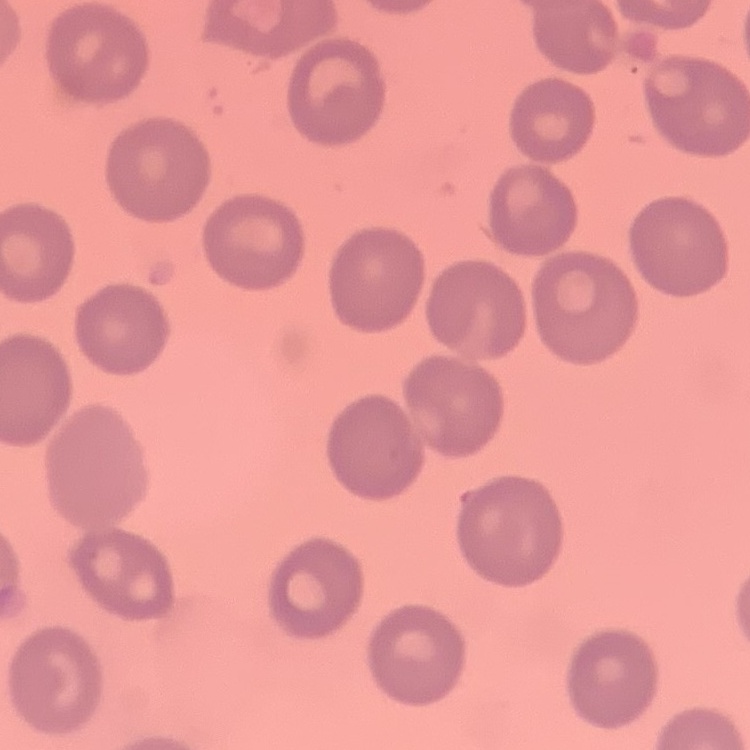
Summary:
  - Erythrocyte morphology: no rouleaux formation
  - Image type: one tile cut from a larger photomicrograph
  - Preparation: thin peripheral smear
  - Stain: Field's or Giemsa